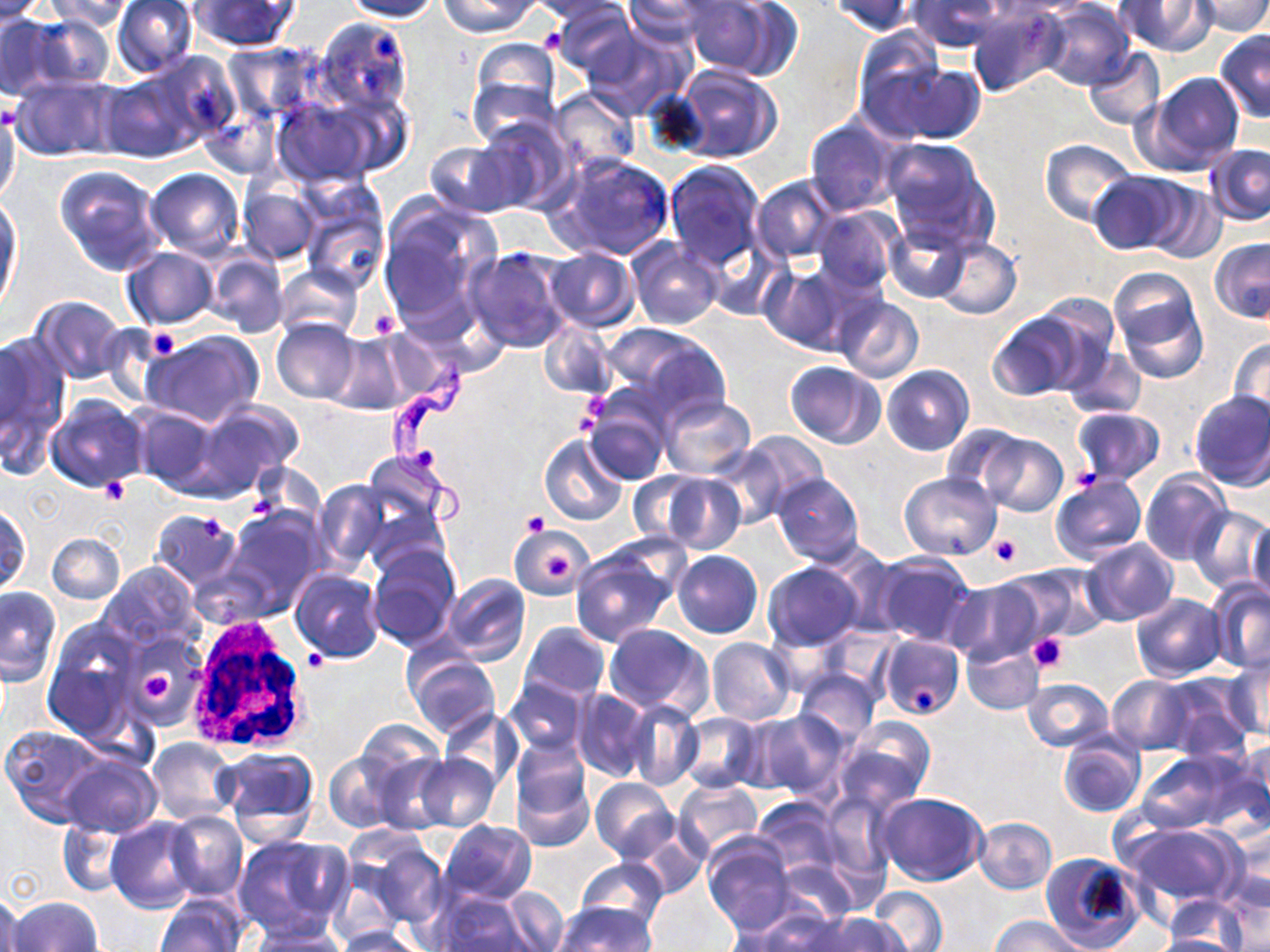

Trypanosoma brucei locations = approximate bounding boxes as named x1/y1/x2/y2 corners in pixels: (x1=384, y1=357, x2=477, y2=526)
slide-level diagnosis = Trypanosoma brucei
modality = light microscopy
white blood cell locations = approximate bounding boxes as named x1/y1/x2/y2 corners in pixels: (x1=194, y1=613, x2=308, y2=746)
preparation = thin blood smear
image size = 1270×952 pixels
magnification = 1000x
platelet locations = approximate bounding boxes as named x1/y1/x2/y2 corners in pixels: (x1=369, y1=309, x2=402, y2=339), (x1=146, y1=328, x2=182, y2=359), (x1=585, y1=392, x2=609, y2=420), (x1=98, y1=478, x2=129, y2=504), (x1=522, y1=512, x2=548, y2=536), (x1=202, y1=517, x2=224, y2=542), (x1=989, y1=535, x2=1021, y2=566), (x1=542, y1=551, x2=570, y2=578), (x1=1028, y1=633, x2=1070, y2=675), (x1=303, y1=650, x2=327, y2=672), (x1=143, y1=668, x2=178, y2=701), (x1=912, y1=686, x2=939, y2=712)
field of view = single
stain = May-Grünwald-Giemsa
uninfected red blood cell locations = approximate bounding boxes as named x1/y1/x2/y2 corners in pixels: (x1=0, y1=0, x2=49, y2=25), (x1=337, y1=0, x2=443, y2=22), (x1=440, y1=0, x2=541, y2=37), (x1=526, y1=0, x2=634, y2=24), (x1=619, y1=0, x2=720, y2=43), (x1=684, y1=0, x2=789, y2=79), (x1=826, y1=0, x2=919, y2=37), (x1=1002, y1=0, x2=1104, y2=14), (x1=1116, y1=0, x2=1217, y2=55), (x1=1193, y1=0, x2=1270, y2=36), (x1=44, y1=1, x2=137, y2=31), (x1=111, y1=1, x2=199, y2=79), (x1=188, y1=1, x2=299, y2=52), (x1=906, y1=1, x2=1010, y2=53), (x1=1038, y1=1, x2=1136, y2=90), (x1=548, y1=2, x2=639, y2=83), (x1=967, y1=5, x2=1065, y2=98), (x1=22, y1=12, x2=116, y2=91), (x1=0, y1=13, x2=63, y2=98), (x1=310, y1=17, x2=416, y2=120), (x1=584, y1=24, x2=693, y2=120), (x1=853, y1=28, x2=947, y2=126), (x1=1215, y1=30, x2=1270, y2=120), (x1=466, y1=39, x2=563, y2=139), (x1=223, y1=43, x2=315, y2=120), (x1=1083, y1=48, x2=1165, y2=130), (x1=97, y1=52, x2=231, y2=163), (x1=866, y1=58, x2=985, y2=145), (x1=670, y1=65, x2=782, y2=163), (x1=1139, y1=72, x2=1246, y2=175), (x1=11, y1=75, x2=122, y2=162), (x1=549, y1=87, x2=640, y2=174), (x1=270, y1=94, x2=385, y2=189), (x1=0, y1=107, x2=21, y2=208), (x1=473, y1=116, x2=576, y2=213), (x1=804, y1=116, x2=902, y2=217), (x1=881, y1=137, x2=995, y2=247), (x1=1040, y1=139, x2=1139, y2=225), (x1=424, y1=141, x2=523, y2=218), (x1=1204, y1=144, x2=1269, y2=225), (x1=553, y1=154, x2=675, y2=260), (x1=663, y1=160, x2=767, y2=270), (x1=55, y1=165, x2=167, y2=276), (x1=146, y1=167, x2=245, y2=258), (x1=1089, y1=172, x2=1192, y2=255), (x1=752, y1=176, x2=840, y2=264), (x1=1142, y1=181, x2=1227, y2=263), (x1=238, y1=184, x2=321, y2=265), (x1=297, y1=192, x2=389, y2=292), (x1=0, y1=199, x2=21, y2=310), (x1=377, y1=199, x2=500, y2=332), (x1=813, y1=206, x2=902, y2=294), (x1=885, y1=221, x2=967, y2=302), (x1=707, y1=235, x2=787, y2=322), (x1=627, y1=237, x2=725, y2=329), (x1=931, y1=237, x2=1022, y2=320), (x1=1209, y1=237, x2=1270, y2=324), (x1=466, y1=246, x2=572, y2=353), (x1=121, y1=248, x2=219, y2=329), (x1=543, y1=249, x2=639, y2=331), (x1=204, y1=250, x2=288, y2=337), (x1=759, y1=262, x2=855, y2=354), (x1=275, y1=264, x2=363, y2=340), (x1=1108, y1=267, x2=1208, y2=382), (x1=834, y1=295, x2=924, y2=384), (x1=32, y1=297, x2=127, y2=385), (x1=985, y1=311, x2=1090, y2=402), (x1=272, y1=318, x2=362, y2=404), (x1=539, y1=320, x2=617, y2=400), (x1=600, y1=322, x2=728, y2=423), (x1=0, y1=330, x2=67, y2=464), (x1=144, y1=331, x2=264, y2=427), (x1=325, y1=332, x2=411, y2=414), (x1=1229, y1=338, x2=1270, y2=428), (x1=1061, y1=342, x2=1147, y2=422), (x1=785, y1=361, x2=885, y2=449), (x1=882, y1=364, x2=974, y2=455), (x1=1188, y1=390, x2=1270, y2=492), (x1=45, y1=395, x2=147, y2=491), (x1=660, y1=395, x2=756, y2=477), (x1=191, y1=398, x2=303, y2=496), (x1=582, y1=398, x2=672, y2=485), (x1=130, y1=404, x2=220, y2=492), (x1=1071, y1=407, x2=1165, y2=484), (x1=942, y1=425, x2=1028, y2=500), (x1=736, y1=430, x2=829, y2=517), (x1=539, y1=434, x2=628, y2=527), (x1=980, y1=434, x2=1067, y2=515), (x1=708, y1=442, x2=792, y2=531), (x1=362, y1=452, x2=451, y2=530), (x1=628, y1=471, x2=713, y2=545), (x1=897, y1=471, x2=1001, y2=561), (x1=1139, y1=471, x2=1229, y2=566), (x1=655, y1=473, x2=746, y2=554), (x1=771, y1=473, x2=865, y2=565), (x1=1050, y1=475, x2=1146, y2=564), (x1=314, y1=480, x2=390, y2=573), (x1=362, y1=497, x2=450, y2=577), (x1=1186, y1=504, x2=1269, y2=594), (x1=1, y1=505, x2=31, y2=595), (x1=222, y1=507, x2=323, y2=615), (x1=149, y1=509, x2=242, y2=592), (x1=1248, y1=516, x2=1269, y2=605), (x1=510, y1=524, x2=590, y2=600), (x1=47, y1=533, x2=124, y2=605), (x1=1080, y1=539, x2=1179, y2=627), (x1=366, y1=545, x2=461, y2=651), (x1=569, y1=545, x2=680, y2=647), (x1=672, y1=550, x2=763, y2=638), (x1=872, y1=551, x2=976, y2=647), (x1=99, y1=562, x2=202, y2=650), (x1=763, y1=562, x2=863, y2=651), (x1=1002, y1=563, x2=1107, y2=643), (x1=290, y1=569, x2=383, y2=661), (x1=442, y1=573, x2=530, y2=666), (x1=944, y1=581, x2=1045, y2=666), (x1=1209, y1=581, x2=1270, y2=672), (x1=0, y1=587, x2=61, y2=686), (x1=1130, y1=594, x2=1226, y2=681), (x1=43, y1=618, x2=142, y2=735), (x1=522, y1=622, x2=610, y2=702), (x1=604, y1=624, x2=712, y2=718), (x1=878, y1=632, x2=965, y2=721), (x1=706, y1=637, x2=796, y2=724), (x1=961, y1=641, x2=1045, y2=715), (x1=405, y1=651, x2=499, y2=739), (x1=1224, y1=659, x2=1269, y2=739), (x1=794, y1=670, x2=879, y2=748), (x1=1155, y1=674, x2=1253, y2=758), (x1=504, y1=675, x2=589, y2=757), (x1=1107, y1=675, x2=1196, y2=753), (x1=1021, y1=677, x2=1113, y2=752), (x1=571, y1=689, x2=655, y2=783), (x1=625, y1=702, x2=703, y2=790), (x1=438, y1=707, x2=522, y2=794), (x1=748, y1=710, x2=851, y2=801), (x1=676, y1=711, x2=764, y2=792), (x1=833, y1=720, x2=933, y2=812), (x1=354, y1=721, x2=446, y2=798), (x1=1, y1=725, x2=109, y2=826), (x1=1057, y1=732, x2=1146, y2=819), (x1=147, y1=737, x2=237, y2=824), (x1=1232, y1=738, x2=1270, y2=833), (x1=509, y1=741, x2=595, y2=851), (x1=217, y1=746, x2=320, y2=845), (x1=1134, y1=750, x2=1252, y2=834), (x1=324, y1=751, x2=400, y2=833), (x1=60, y1=753, x2=160, y2=835), (x1=413, y1=753, x2=498, y2=831), (x1=590, y1=777, x2=679, y2=863), (x1=674, y1=780, x2=764, y2=860), (x1=818, y1=792, x2=896, y2=886), (x1=877, y1=792, x2=986, y2=885), (x1=752, y1=798, x2=843, y2=879), (x1=164, y1=811, x2=248, y2=900), (x1=974, y1=816, x2=1056, y2=894), (x1=106, y1=818, x2=201, y2=913), (x1=58, y1=819, x2=133, y2=896), (x1=438, y1=820, x2=536, y2=904), (x1=1116, y1=822, x2=1245, y2=914), (x1=1220, y1=824, x2=1270, y2=918), (x1=630, y1=826, x2=709, y2=899), (x1=345, y1=832, x2=448, y2=935), (x1=232, y1=835, x2=349, y2=937), (x1=702, y1=835, x2=798, y2=936), (x1=1042, y1=853, x2=1144, y2=952), (x1=576, y1=857, x2=668, y2=929), (x1=869, y1=886, x2=947, y2=952), (x1=491, y1=889, x2=571, y2=951), (x1=432, y1=891, x2=544, y2=951), (x1=0, y1=893, x2=22, y2=952), (x1=158, y1=895, x2=247, y2=952), (x1=10, y1=897, x2=102, y2=952), (x1=1163, y1=899, x2=1248, y2=948), (x1=553, y1=903, x2=655, y2=952), (x1=730, y1=910, x2=839, y2=952), (x1=804, y1=913, x2=906, y2=952), (x1=988, y1=916, x2=1086, y2=952), (x1=244, y1=925, x2=351, y2=952), (x1=331, y1=926, x2=426, y2=952), (x1=1152, y1=933, x2=1245, y2=952)